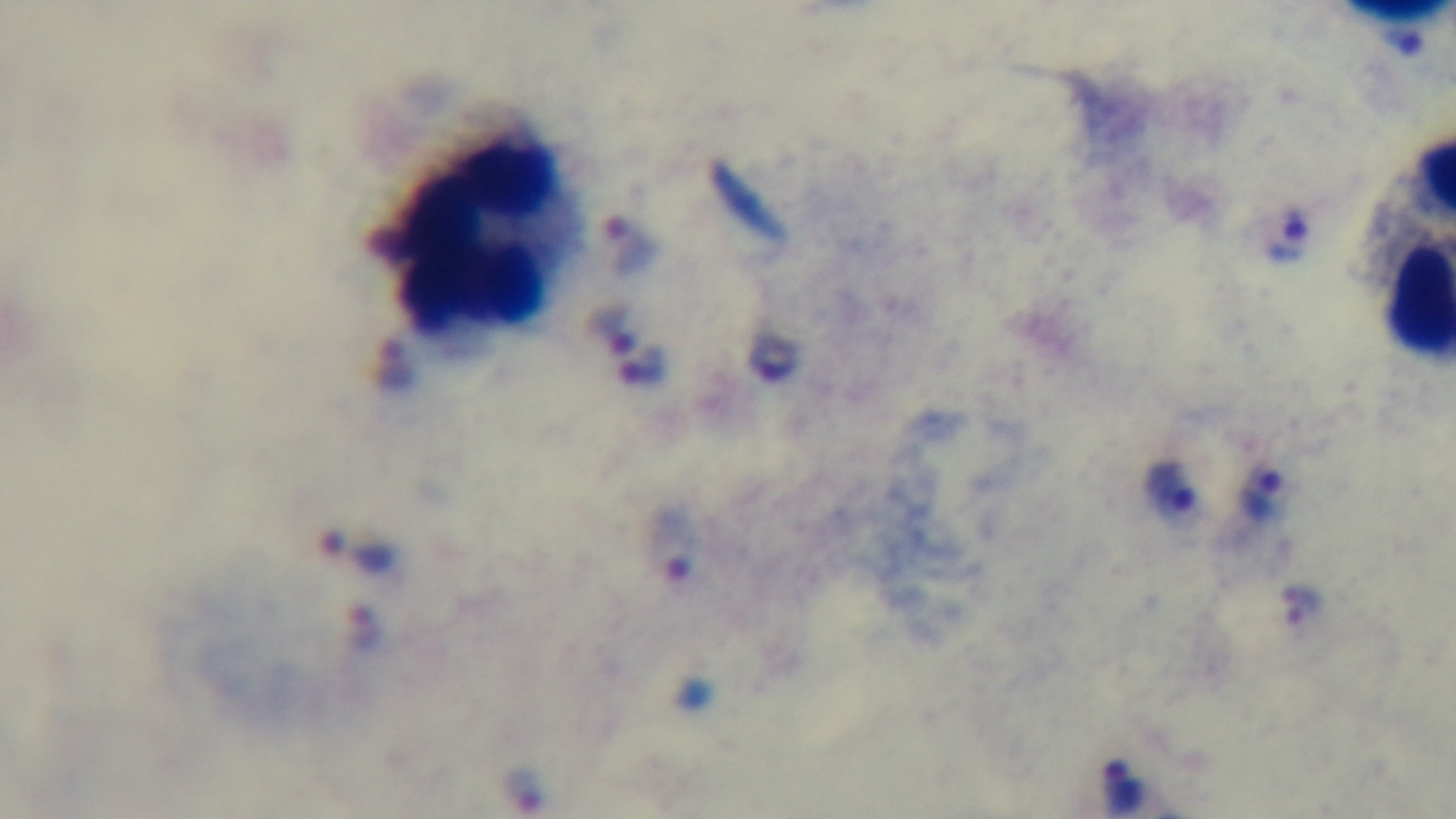
malaria_status: positive
field_of_view: one from the slide
modality: light microscopy
preparation: thick
objective: 100x oil immersion
capture: mounted 4K digital camera
stain: Giemsa